Classify this cell by malaria status.
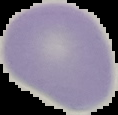

It is uninfected.

Summary:
  - Image type: cell region segmented out of the field of view; surrounding area masked to black
  - Image size: 118×115 pixels
  - Preparation: thin blood film